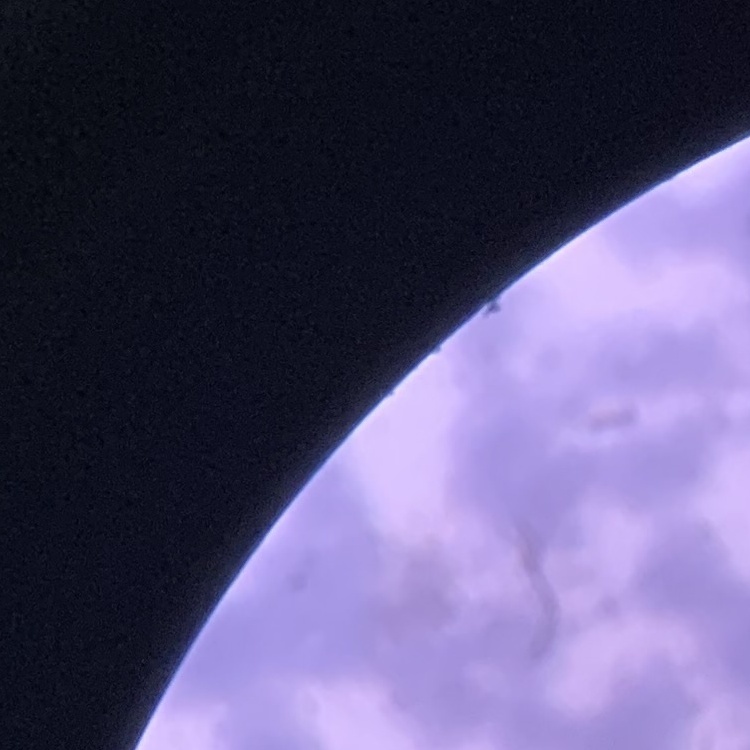
erythrocyte morphology = rouleaux formation
preparation = thin blood film
image type = square crop of a larger photomicrograph
stain = Field's or Giemsa